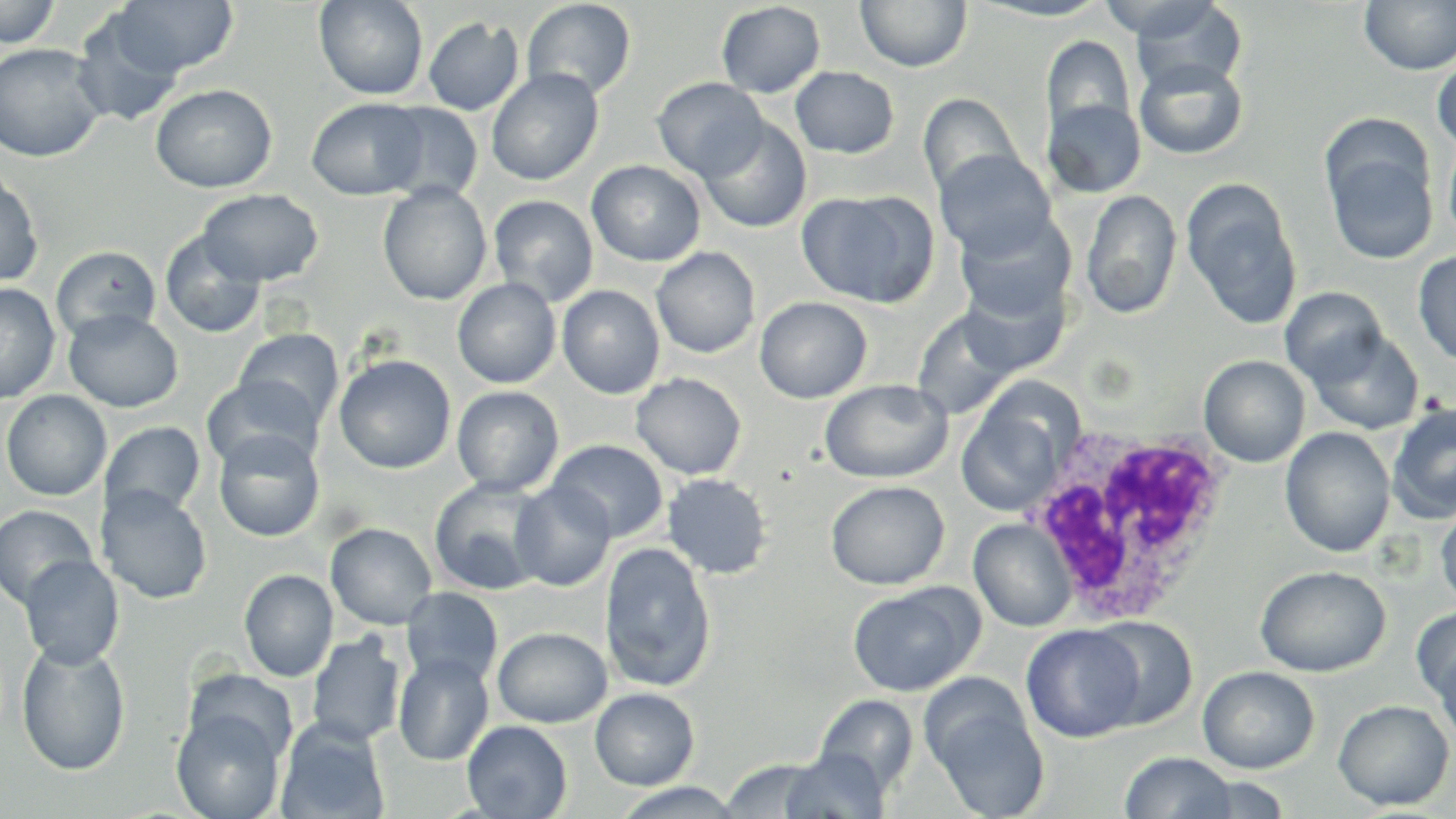
slide-level diagnosis = Plasmodium ovale
magnification = 1000x
stain = May-Grünwald-Giemsa
uninfected red blood cell locations = approximate bounding boxes as named x1/y1/x2/y2 corners in pixels: (x1=0, y1=0, x2=62, y2=49), (x1=112, y1=0, x2=238, y2=77), (x1=314, y1=0, x2=429, y2=100), (x1=855, y1=0, x2=972, y2=73), (x1=970, y1=0, x2=1117, y2=22), (x1=1128, y1=0, x2=1248, y2=95), (x1=1359, y1=0, x2=1456, y2=76), (x1=522, y1=1, x2=637, y2=101), (x1=716, y1=2, x2=825, y2=98), (x1=71, y1=10, x2=186, y2=128), (x1=423, y1=16, x2=524, y2=115), (x1=1040, y1=35, x2=1136, y2=139), (x1=0, y1=42, x2=107, y2=162), (x1=1432, y1=54, x2=1456, y2=152), (x1=1134, y1=57, x2=1249, y2=160), (x1=790, y1=66, x2=900, y2=158), (x1=486, y1=68, x2=604, y2=186), (x1=652, y1=77, x2=767, y2=181), (x1=150, y1=84, x2=277, y2=193), (x1=918, y1=93, x2=1025, y2=199), (x1=306, y1=97, x2=429, y2=200), (x1=1043, y1=98, x2=1146, y2=197), (x1=378, y1=102, x2=483, y2=203), (x1=698, y1=118, x2=811, y2=233), (x1=1322, y1=130, x2=1439, y2=266), (x1=1442, y1=130, x2=1456, y2=249), (x1=934, y1=149, x2=1056, y2=261), (x1=586, y1=160, x2=706, y2=266), (x1=0, y1=169, x2=43, y2=289), (x1=1182, y1=178, x2=1302, y2=331), (x1=378, y1=181, x2=492, y2=305), (x1=197, y1=189, x2=323, y2=286), (x1=797, y1=189, x2=941, y2=308), (x1=1080, y1=189, x2=1182, y2=320), (x1=488, y1=195, x2=599, y2=307), (x1=953, y1=212, x2=1075, y2=324), (x1=159, y1=230, x2=266, y2=339), (x1=51, y1=246, x2=162, y2=343), (x1=651, y1=247, x2=760, y2=358), (x1=1412, y1=251, x2=1456, y2=366), (x1=954, y1=273, x2=1070, y2=378), (x1=452, y1=277, x2=561, y2=388), (x1=0, y1=283, x2=60, y2=405), (x1=557, y1=285, x2=665, y2=399), (x1=1281, y1=287, x2=1388, y2=387), (x1=754, y1=297, x2=872, y2=403), (x1=911, y1=307, x2=1022, y2=420), (x1=64, y1=309, x2=183, y2=413), (x1=1304, y1=325, x2=1425, y2=436), (x1=235, y1=328, x2=344, y2=430), (x1=334, y1=354, x2=457, y2=474), (x1=1199, y1=355, x2=1310, y2=467), (x1=630, y1=372, x2=747, y2=479), (x1=201, y1=375, x2=323, y2=472), (x1=819, y1=378, x2=954, y2=484), (x1=451, y1=385, x2=564, y2=496), (x1=1, y1=390, x2=111, y2=501), (x1=1386, y1=403, x2=1456, y2=523), (x1=957, y1=405, x2=1067, y2=516), (x1=100, y1=421, x2=206, y2=521), (x1=1280, y1=427, x2=1395, y2=558), (x1=214, y1=429, x2=324, y2=542), (x1=548, y1=439, x2=668, y2=542), (x1=661, y1=472, x2=773, y2=579), (x1=429, y1=477, x2=549, y2=596), (x1=510, y1=480, x2=616, y2=591), (x1=825, y1=480, x2=949, y2=589), (x1=97, y1=485, x2=213, y2=605), (x1=1435, y1=498, x2=1456, y2=612), (x1=0, y1=504, x2=97, y2=611), (x1=968, y1=518, x2=1076, y2=632), (x1=325, y1=523, x2=437, y2=630), (x1=599, y1=541, x2=717, y2=692), (x1=19, y1=555, x2=124, y2=669), (x1=1255, y1=565, x2=1391, y2=677), (x1=239, y1=569, x2=339, y2=682), (x1=847, y1=582, x2=982, y2=697), (x1=401, y1=587, x2=504, y2=688), (x1=1411, y1=605, x2=1456, y2=711), (x1=1088, y1=615, x2=1197, y2=730), (x1=1021, y1=624, x2=1144, y2=742), (x1=493, y1=626, x2=612, y2=728), (x1=306, y1=632, x2=406, y2=747), (x1=1431, y1=635, x2=1456, y2=747), (x1=17, y1=639, x2=131, y2=776), (x1=393, y1=652, x2=494, y2=766), (x1=1198, y1=666, x2=1319, y2=774), (x1=590, y1=688, x2=699, y2=790), (x1=926, y1=690, x2=1049, y2=818), (x1=813, y1=694, x2=919, y2=795), (x1=1333, y1=699, x2=1454, y2=810), (x1=172, y1=705, x2=287, y2=819), (x1=276, y1=719, x2=390, y2=819), (x1=462, y1=720, x2=572, y2=819), (x1=778, y1=747, x2=890, y2=819), (x1=1119, y1=751, x2=1238, y2=818), (x1=719, y1=757, x2=829, y2=817), (x1=1185, y1=774, x2=1292, y2=818), (x1=610, y1=782, x2=745, y2=818)
modality = light microscopy
white blood cell locations = approximate bounding boxes as named x1/y1/x2/y2 corners in pixels: (x1=1027, y1=424, x2=1237, y2=626)
field of view = one of a larger specimen
preparation = thin blood smear
image size = 1456×819 pixels